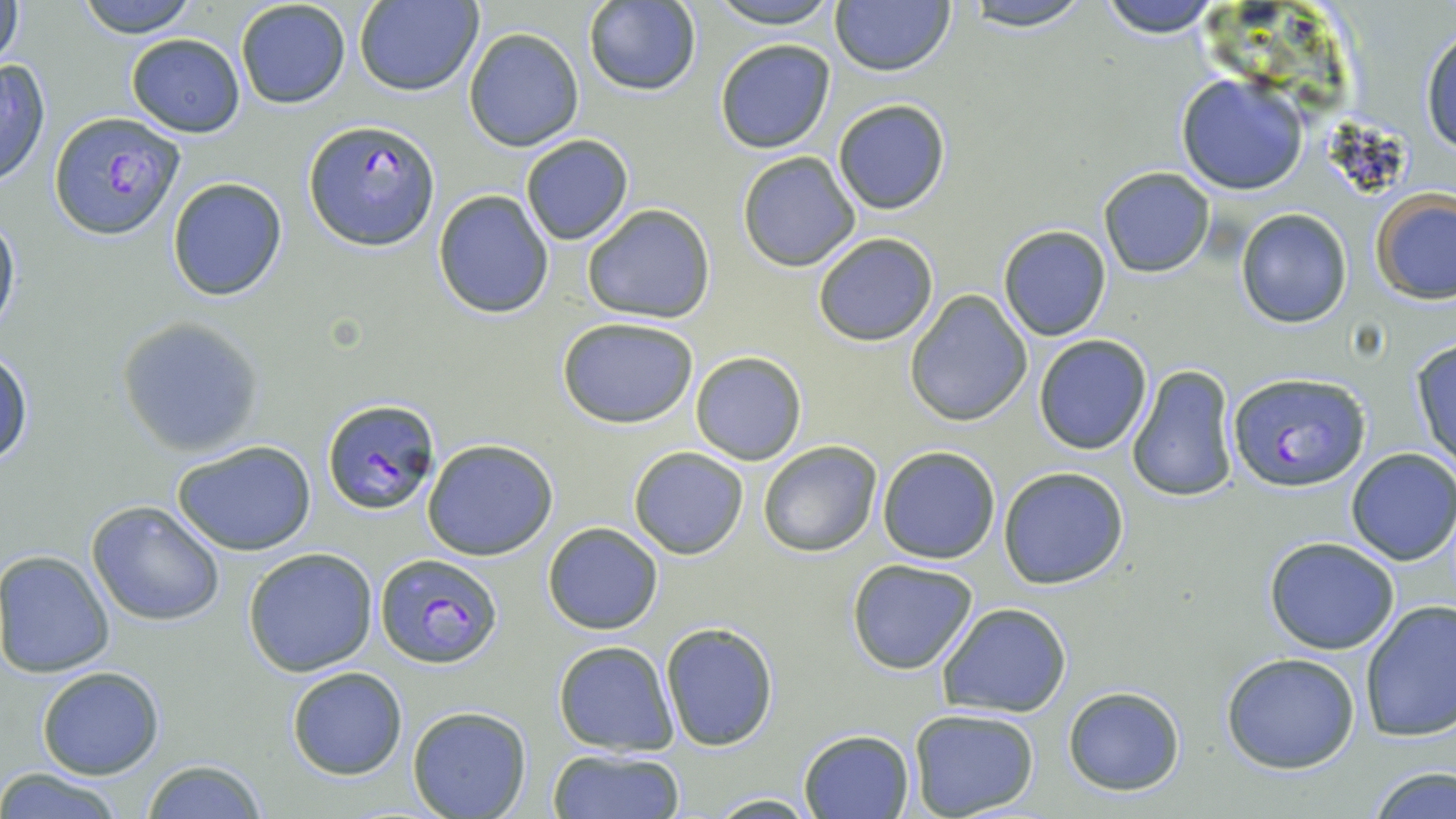

Summary:
  - Coordinate format: approximate bounding boxes as (x1,y1)-(x2,y2) corner pairs in pixels
  - Plasmodium falciparum-infected red blood cell locations: (49,111)-(186,239), (305,118)-(439,251), (1226,370)-(1372,492), (322,397)-(439,516), (374,552)-(504,668)
  - Uninfected red blood cell locations: (1,0)-(26,71), (75,0)-(199,36), (355,0)-(482,96), (583,0)-(701,96), (704,0)-(843,29), (963,0)-(1094,32), (1095,0)-(1230,38), (235,1)-(351,110), (830,1)-(955,77), (1420,23)-(1456,156), (463,27)-(584,150), (126,33)-(245,138), (714,39)-(835,153), (0,59)-(50,189), (1175,73)-(1309,196), (832,97)-(951,214), (520,134)-(633,245), (737,152)-(859,272), (1098,168)-(1213,278), (166,177)-(288,301), (433,189)-(556,319), (1370,190)-(1456,305), (581,203)-(715,322), (1236,208)-(1354,327), (0,211)-(21,340), (996,224)-(1112,341), (813,233)-(939,347), (904,290)-(1034,427), (118,316)-(265,455), (556,316)-(701,428), (1034,335)-(1152,455), (1409,337)-(1456,469), (1,346)-(34,469), (690,351)-(807,465), (1126,363)-(1240,505), (423,438)-(556,560), (171,439)-(317,557), (758,439)-(882,558), (877,445)-(1001,564), (627,446)-(750,560), (1345,448)-(1456,565), (998,466)-(1129,590), (87,500)-(226,626), (542,522)-(664,635), (1262,536)-(1401,655), (243,547)-(378,677), (0,549)-(115,678), (846,558)-(981,675), (1359,601)-(1456,743), (937,602)-(1073,717), (660,622)-(779,751), (552,640)-(678,754), (1223,653)-(1361,773), (37,666)-(165,780), (286,667)-(408,780), (1063,685)-(1186,795), (407,707)-(531,819), (908,708)-(1041,818), (798,728)-(914,818), (547,748)-(686,819), (137,760)-(267,817), (0,767)-(127,819), (1365,767)-(1456,819), (706,793)-(821,818)
  - Slide-level diagnosis: Plasmodium falciparum
  - Image size: 1456×819 pixels
  - Modality: light microscopy
  - Preparation: thin blood smear
  - Magnification: 1000x
  - Field of view: single
  - Stain: May-Grünwald-Giemsa